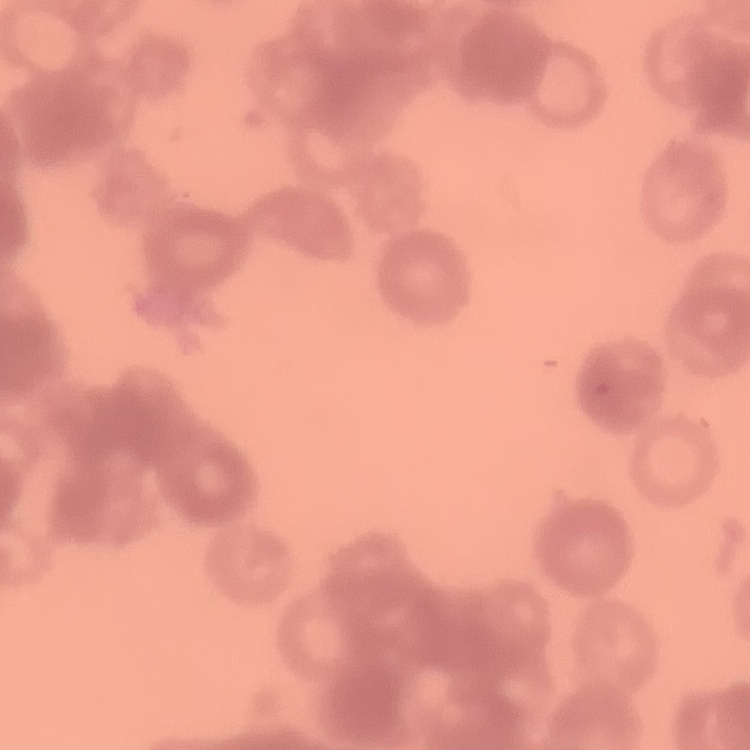

Summary:
  - Red blood cell morphology: rouleaux formation
  - Image type: square crop of a larger photomicrograph
  - Preparation: thin peripheral smear
  - Stain: Field's or Giemsa